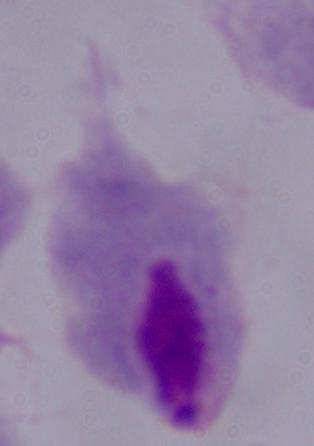
Captured at 1000x magnification. A trichomonad is shown. Photomicrograph.